Assess the morphology of the red blood cells.
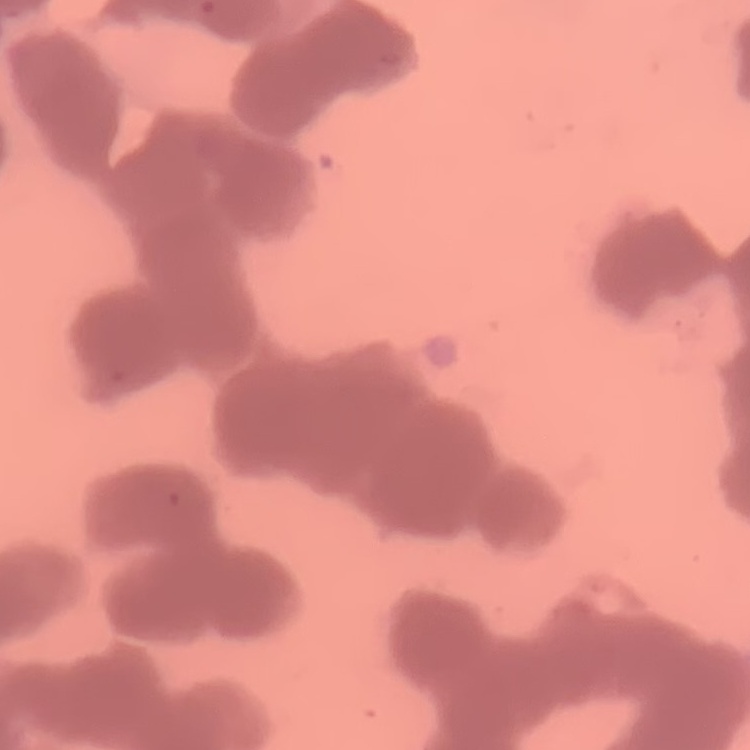

They show rouleaux formation.

stain = Field's or Giemsa
image type = square crop of a larger photomicrograph
preparation = thin blood film